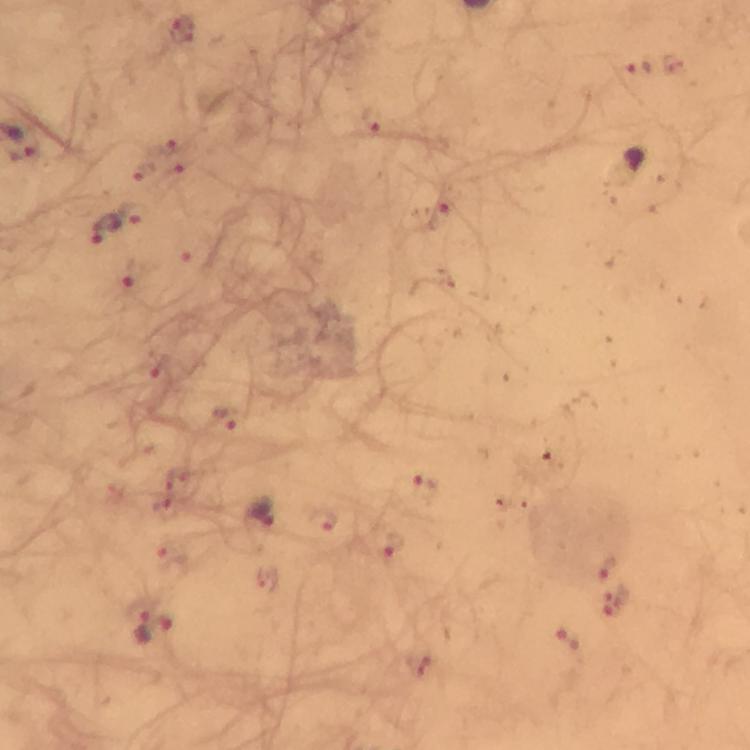
Approximate centers as {x, y} in pixels.
Summary:
  - Plasmodium parasite locations: {182, 28}, {637, 67}, {370, 121}, {633, 161}, {134, 213}, {104, 232}, {135, 275}, {225, 420}, {425, 488}, {262, 514}, {392, 544}, {608, 567}, {143, 625}, {567, 639}
  - Image size: 750×750 pixels
  - Preparation: thick blood film
  - Immersion oil: applied
  - Magnification: 100x
  - Context: from a diagnostic examination for malaria
  - Stain: Giemsa
  - Cropped from: one field of view
  - Capture: smartphone photograph through a microscope